Look for Plasmodium parasites.
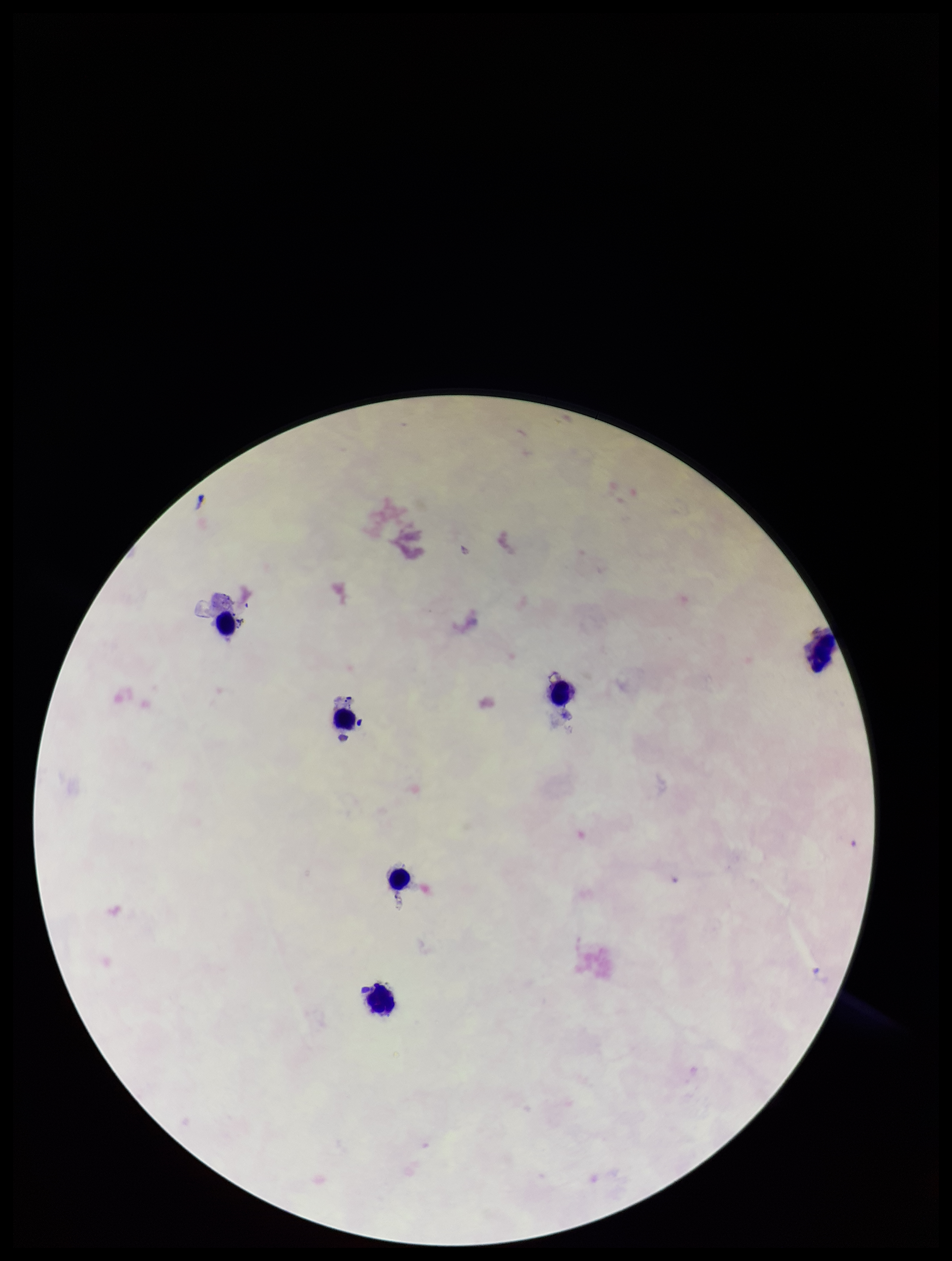

None detected.

Single field of view. Photographed through the microscope eyepiece with a smartphone camera. Leukocyte count: 6. Image is 952×1261 pixels. Preparation: thick. Parasite count: 0. Patient malaria status: negative. Stained with Giemsa.